Rate the background quality.
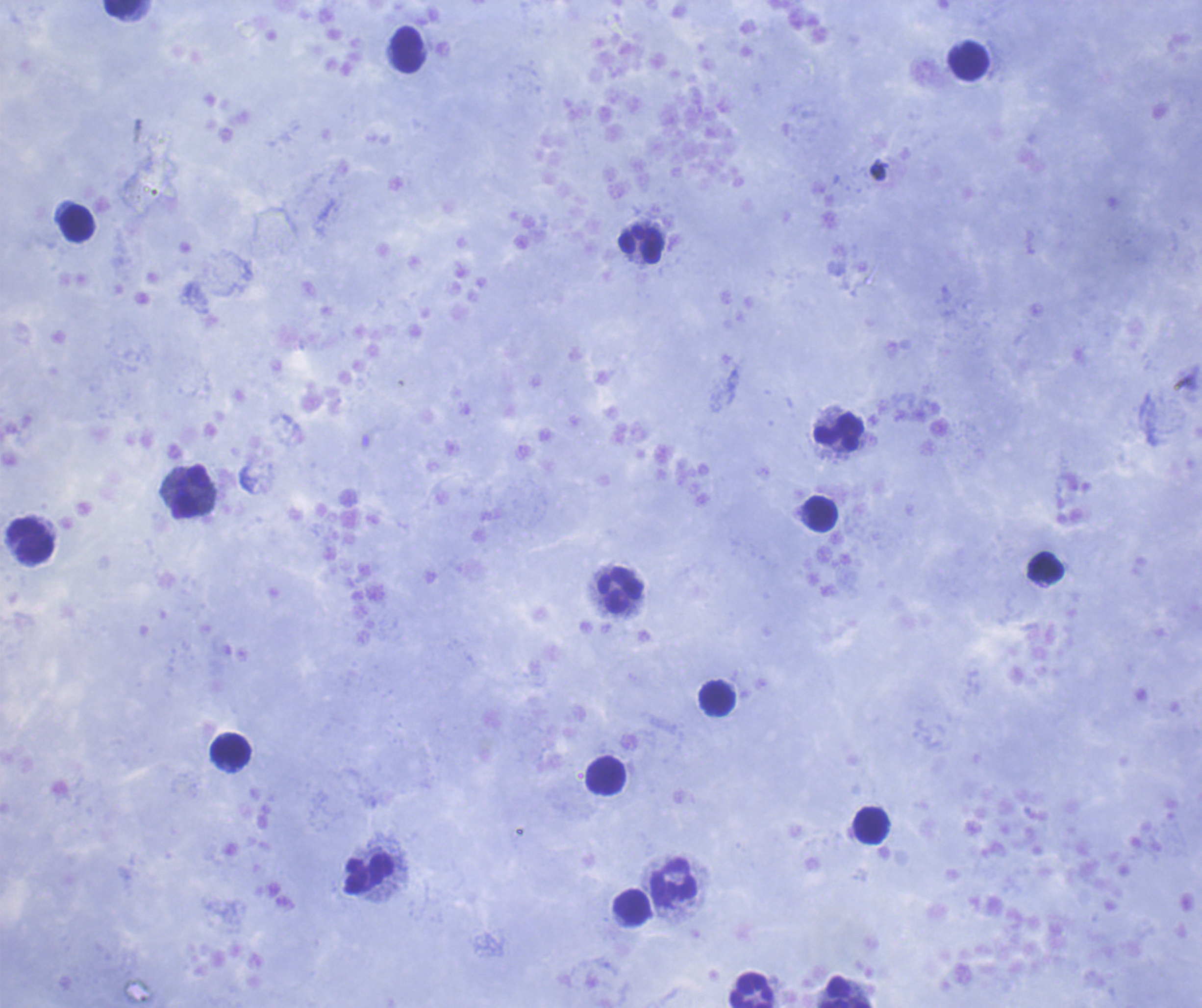

Satisfactory.

Approximate object centers, in pixels from the top-left corner.
Summary:
  - Leukocyte locations: (x=122, y=9), (x=407, y=50), (x=968, y=60), (x=77, y=224), (x=641, y=245), (x=838, y=431), (x=192, y=491), (x=820, y=515), (x=31, y=540), (x=1045, y=568), (x=620, y=590), (x=718, y=697), (x=230, y=750), (x=606, y=775), (x=870, y=825), (x=369, y=875), (x=674, y=884), (x=632, y=907), (x=752, y=989), (x=845, y=992)
  - Field of view: one from this slide
  - Image size: 1202×1008 pixels
  - Magnification: 100x
  - Preparation: thick blood film
  - Coloration quality: good
  - Stain: Romanowsky
  - Result: no malaria parasites seen
  - Context: previously used in an actual diagnosis